Report the malaria status of this cell.
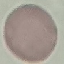
Uninfected.

Cell patch, automatically extracted from a larger field of view and resized to 64 × 64 pixels. Giemsa stain. Acquired by smartphone through the microscope eyepiece. Thin blood smear.